Assess this cell for malaria.
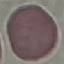
Uninfected.

Thin smear of blood. Acquired by smartphone through the microscope eyepiece. Giemsa-stained preparation. Automatically extracted cell patch, resized to 64 × 64 pixels.